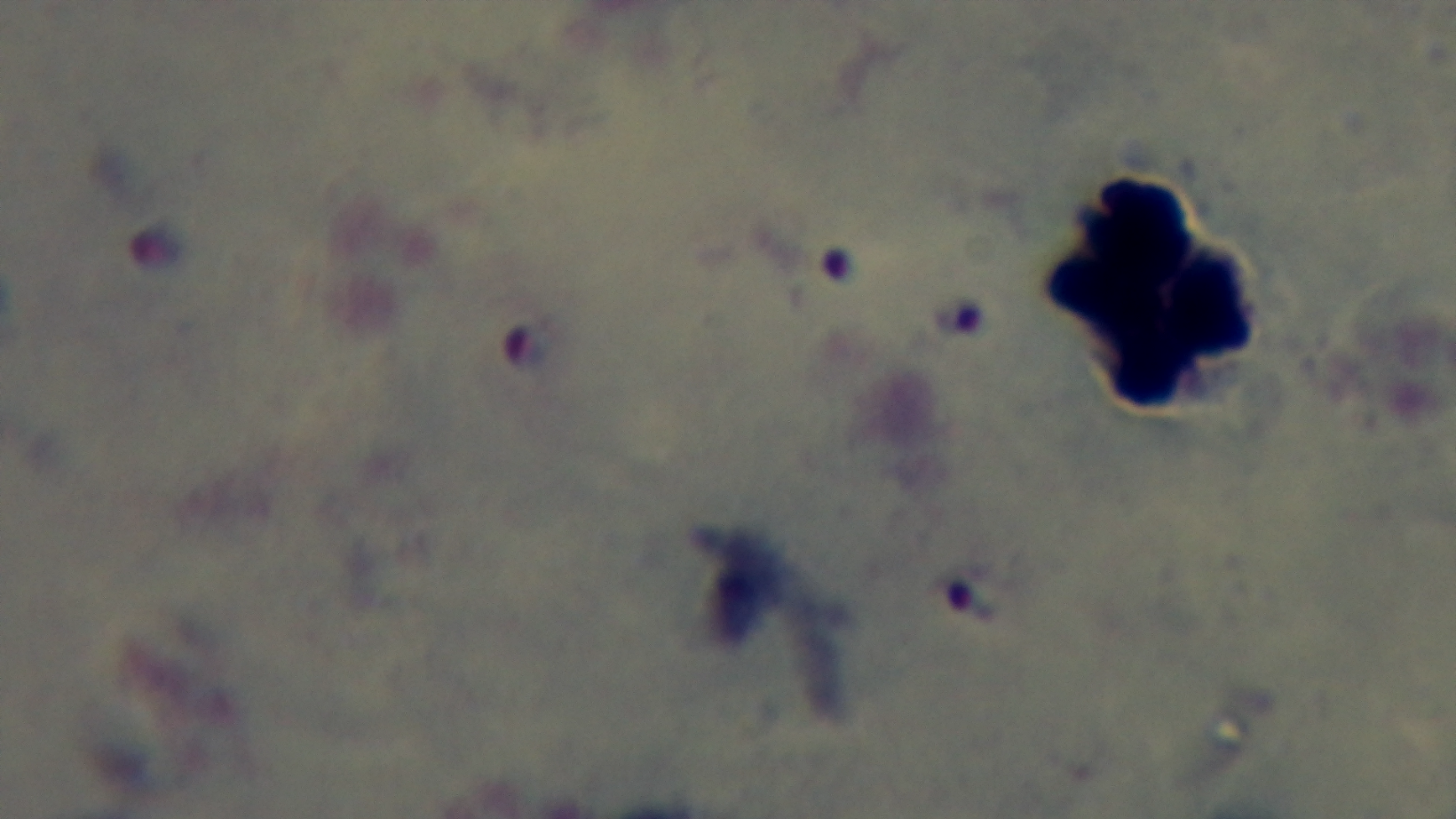 Preparation: thick blood film. Giemsa stain. Photomicrograph. 100x oil-immersion objective. Mounted 4K digital camera. Single field of view. Malaria status: positive.